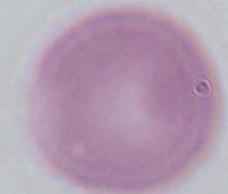

Captured at 1000x magnification. Photomicrograph. A red blood cell is shown.